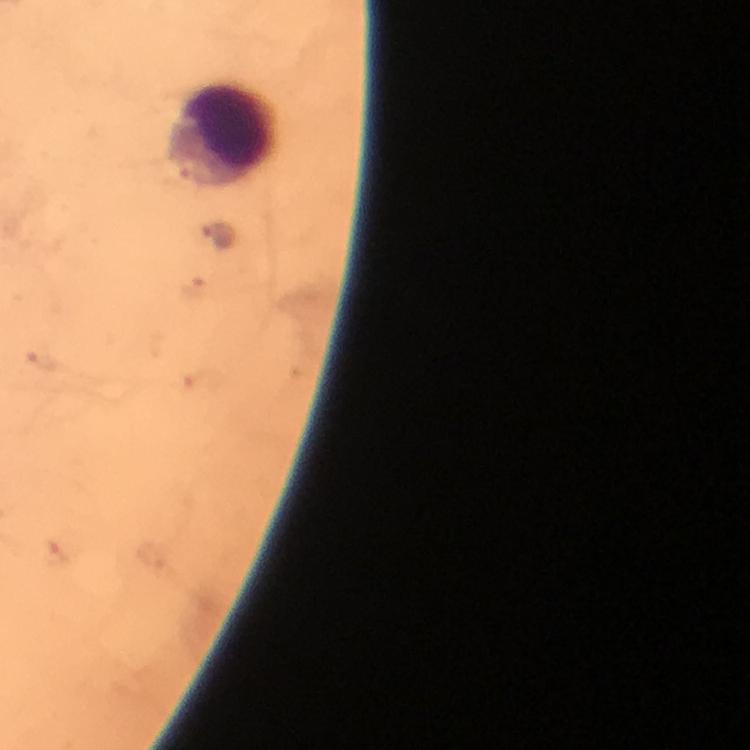

Approximate object centers, in pixels from the top-left corner.
Summary:
  - Malaria parasite locations: (x=218, y=237), (x=42, y=359)
  - Leukocyte locations: (x=226, y=136)
  - Stain: Giemsa
  - Preparation: thick blood film
  - Magnification: 100x
  - Image size: 750×750 pixels
  - Immersion oil: applied
  - Capture: smartphone photograph through a microscope
  - Context: from a malaria diagnostic workup
  - Cropped from: a single field of view